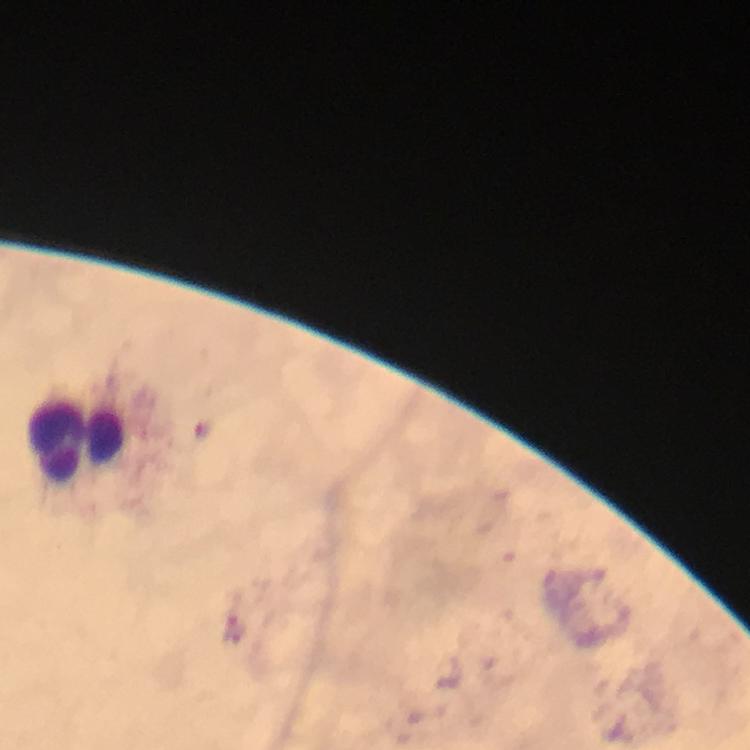
capture: smartphone mounted on the microscope
immersion_oil: used
leukocyte_locations: 'approximate object centers, in pixels from the top-left corner: (x=77, y=444)'
preparation: thick smear
cropped_from: a single field of view
magnification: 100x
context: from a diagnostic examination for malaria
stain: Giemsa
malaria_parasite_locations: 'approximate object centers, in pixels from the top-left corner: (x=234, y=629)'
image_size: 750×750 pixels